Locate and identify every blood parasite.
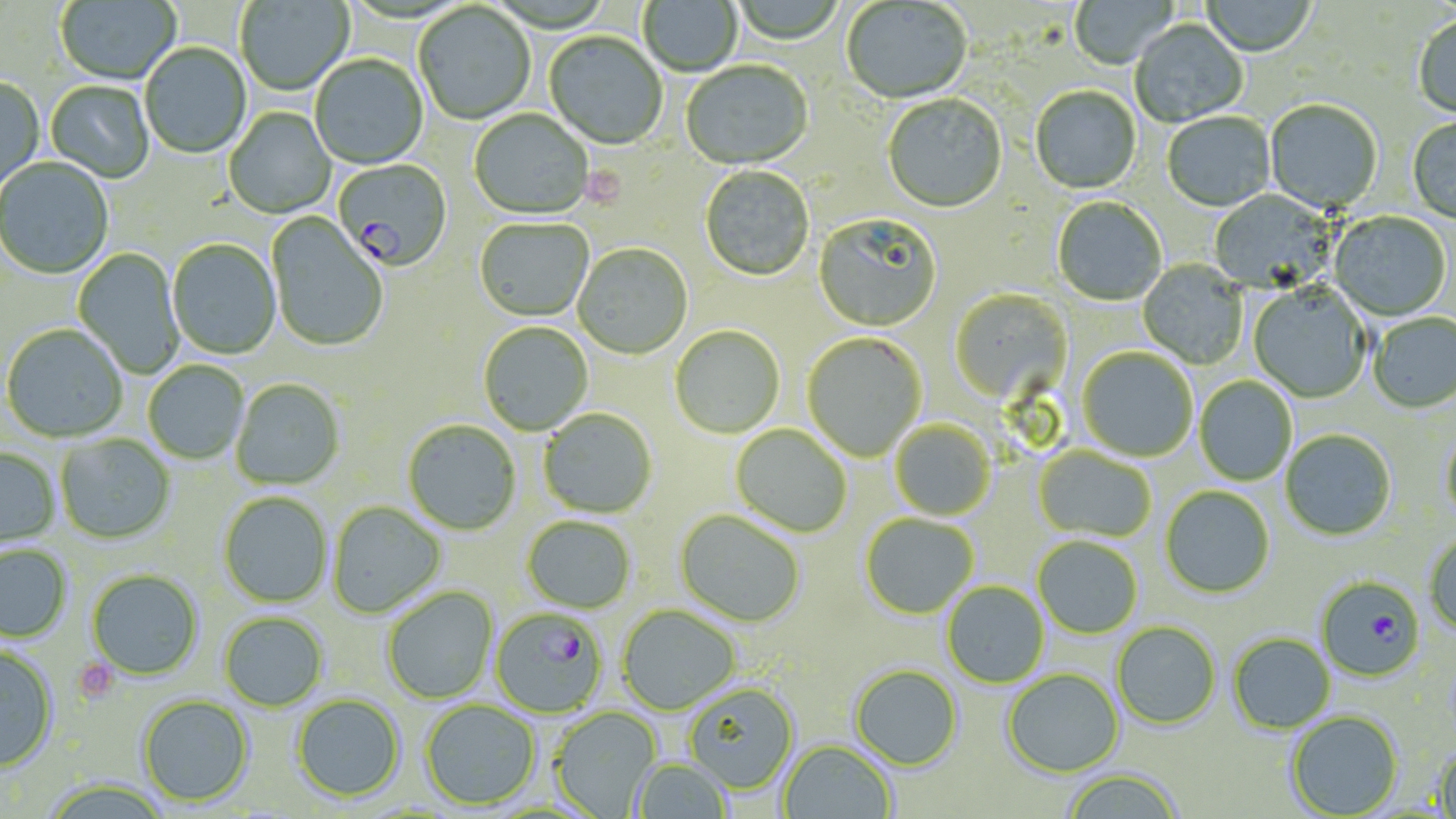

Approximate bounding boxes as (x1,y1)-(x2,y2) corner pairs in pixels.
Plasmodium falciparum-infected red blood cells: (333,159)-(453,273), (1315,576)-(1426,683), (492,607)-(608,717).
No Plasmodium ovale, Plasmodium malariae, Plasmodium vivax, Babesia divergens, or Trypanosoma brucei observed.

Uninfected red blood cell locations: (55,0)-(181,87), (235,0)-(355,97), (1070,0)-(1178,70), (1201,0)-(1316,58), (638,1)-(742,77), (730,1)-(846,46), (841,1)-(973,105), (414,4)-(536,126), (1413,16)-(1456,119), (1130,21)-(1248,128), (544,32)-(667,151), (140,43)-(252,160), (310,56)-(428,170), (681,62)-(813,172), (0,77)-(45,197), (45,81)-(154,183), (1030,87)-(1141,195), (883,95)-(1008,215), (1265,100)-(1382,214), (224,107)-(336,220), (469,110)-(593,221), (1162,113)-(1276,213), (1407,118)-(1456,225), (0,158)-(113,281), (699,166)-(814,282), (1210,190)-(1337,294), (1052,198)-(1167,307), (1329,212)-(1451,322), (266,213)-(388,353), (813,215)-(942,333), (475,219)-(593,323), (167,240)-(282,361), (572,244)-(693,360), (73,247)-(184,379), (1138,260)-(1248,370), (1248,283)-(1371,404), (951,289)-(1072,406), (1368,313)-(1456,414), (478,322)-(593,436), (2,324)-(128,442), (670,326)-(785,439), (802,333)-(927,462), (1077,348)-(1198,462), (143,362)-(249,464), (1195,376)-(1297,486), (231,380)-(344,491), (538,409)-(656,519), (403,420)-(521,536), (890,421)-(995,521), (731,425)-(852,537), (1280,429)-(1396,541), (1440,429)-(1456,530), (56,434)-(175,545), (1034,447)-(1156,543), (0,449)-(60,551), (1160,486)-(1275,599), (218,492)-(332,608), (327,501)-(446,618), (675,510)-(804,627), (860,513)-(978,619), (522,516)-(636,614), (1424,532)-(1456,637), (1033,536)-(1143,639), (0,544)-(73,643), (86,569)-(203,680), (942,582)-(1049,687), (382,586)-(498,704), (617,605)-(740,715), (219,612)-(328,711), (1112,621)-(1221,729), (1228,633)-(1335,733), (0,646)-(59,772), (849,664)-(963,770), (1002,669)-(1124,778), (684,682)-(800,794), (291,693)-(405,802), (137,694)-(255,806), (420,700)-(540,809), (550,707)-(662,817), (1286,710)-(1403,817), (779,740)-(897,819), (1432,744)-(1456,817), (632,759)-(733,818), (1062,769)-(1184,819), (40,779)-(173,819). Platelet locations: (579,167)-(627,210), (72,657)-(118,703). Slide-level diagnosis: Plasmodium falciparum. 1000x magnification. Light microscopy. May-Grünwald-Giemsa stain. One field of a larger specimen. Thin blood smear. Image is 1456×819 pixels.